Name the parasite shown.
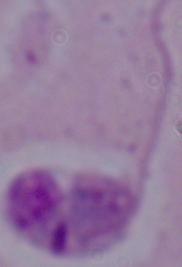

Leishmania.

Summary:
  - Magnification: 1000x
  - Modality: photomicrograph